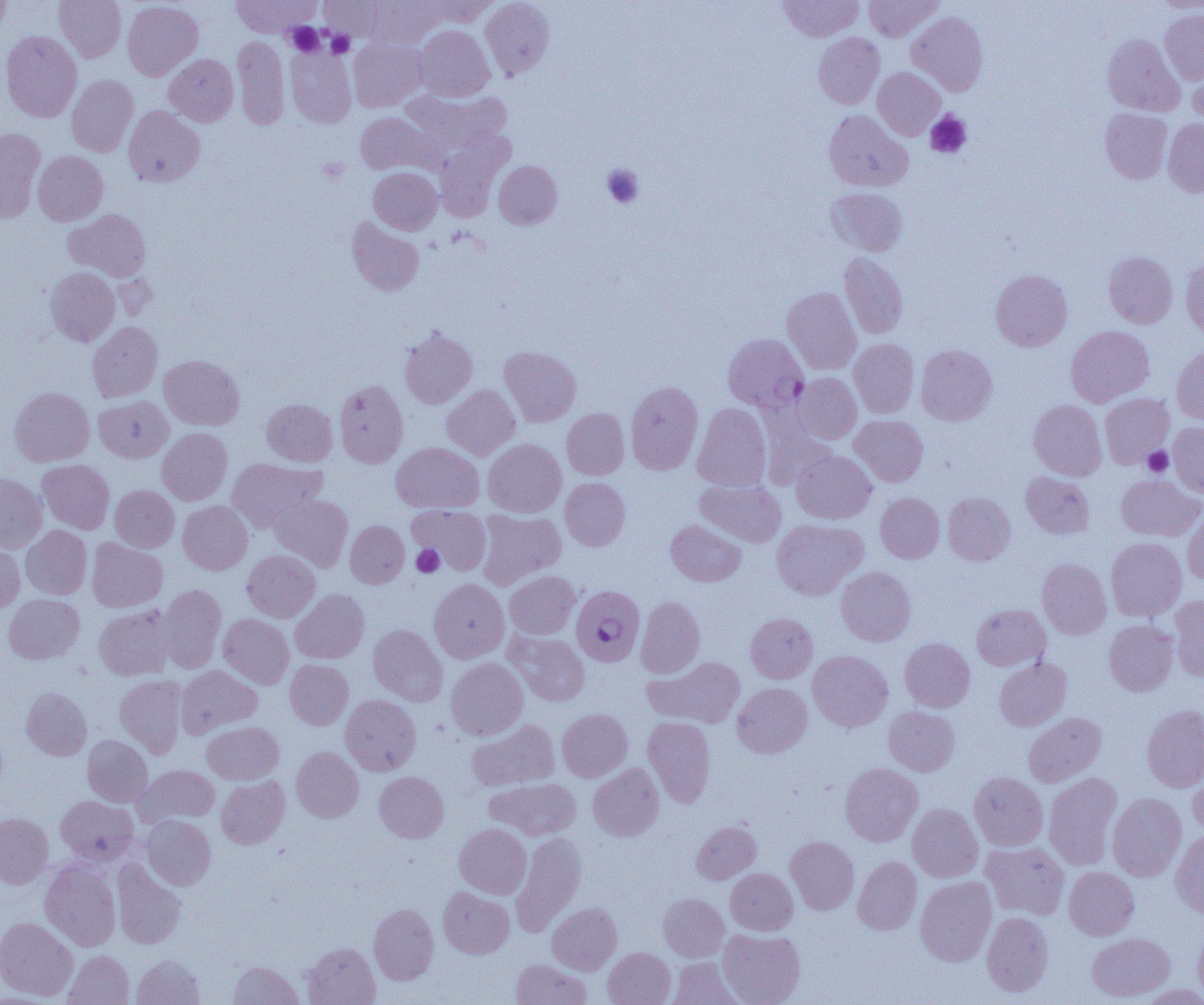

Summary:
  - Coordinate format: approximate bounding boxes as (x1, y1, x2, y2) in pixels
  - Uninfected red blood cell locations: (0, 0, 11, 40), (54, 0, 126, 62), (230, 0, 319, 37), (320, 0, 389, 41), (480, 0, 555, 80), (778, 0, 863, 41), (864, 0, 943, 40), (1153, 0, 1204, 12), (123, 1, 203, 80), (366, 1, 446, 49), (422, 1, 499, 26), (1160, 9, 1204, 85), (907, 12, 988, 96), (415, 26, 494, 101), (1, 31, 82, 122), (813, 32, 884, 109), (1102, 34, 1184, 116), (232, 36, 289, 130), (349, 38, 428, 112), (285, 45, 357, 128), (164, 54, 238, 126), (1187, 62, 1204, 126), (873, 67, 945, 140), (66, 74, 139, 157), (404, 89, 511, 155), (123, 105, 205, 187), (1100, 108, 1173, 184), (824, 110, 912, 191), (355, 112, 439, 175), (1163, 119, 1204, 197), (0, 128, 45, 222), (435, 138, 510, 222), (33, 151, 108, 225), (494, 160, 562, 229), (368, 167, 441, 234), (827, 187, 908, 257), (65, 209, 151, 280), (347, 217, 424, 296), (1103, 251, 1178, 328), (839, 253, 908, 339), (1180, 255, 1204, 337), (45, 267, 120, 346), (991, 269, 1072, 351), (782, 287, 861, 374), (87, 322, 163, 402), (1065, 326, 1154, 407), (399, 327, 478, 408), (849, 338, 919, 417), (1171, 343, 1204, 425), (916, 345, 997, 425), (499, 346, 581, 426), (159, 354, 244, 430), (793, 373, 862, 444), (334, 379, 408, 468), (626, 381, 703, 474), (442, 384, 520, 460), (9, 387, 94, 466), (1100, 393, 1174, 468), (94, 396, 173, 462), (262, 399, 337, 466), (1028, 399, 1107, 480), (692, 403, 772, 491), (562, 408, 629, 479), (850, 415, 928, 487), (1168, 421, 1204, 496), (157, 427, 232, 505), (483, 439, 566, 517), (391, 442, 484, 513), (791, 450, 876, 524), (227, 457, 325, 532), (37, 459, 114, 533), (1020, 472, 1095, 539), (0, 473, 47, 553), (1115, 474, 1203, 541), (560, 477, 630, 550), (695, 478, 786, 547), (110, 485, 179, 552), (875, 492, 944, 563), (943, 492, 1015, 565), (270, 493, 353, 571), (178, 501, 252, 574), (408, 505, 491, 575), (476, 509, 566, 589), (1183, 509, 1204, 585), (666, 519, 746, 586), (771, 519, 867, 600), (345, 520, 409, 588), (21, 525, 92, 600), (1106, 537, 1187, 621), (87, 538, 167, 612), (0, 541, 25, 613), (242, 550, 320, 622), (1037, 557, 1111, 639), (836, 566, 916, 646), (504, 571, 580, 639), (429, 579, 509, 663), (158, 584, 226, 673), (291, 588, 370, 664), (3, 594, 84, 664), (636, 596, 705, 678), (1169, 596, 1204, 680), (972, 604, 1050, 670), (94, 605, 175, 680), (218, 613, 294, 688), (746, 613, 817, 683), (1104, 619, 1178, 696), (368, 625, 447, 705), (508, 632, 589, 706), (899, 638, 975, 712), (807, 650, 893, 732), (645, 656, 745, 728), (446, 658, 528, 740), (994, 658, 1071, 731), (285, 659, 353, 729), (176, 665, 262, 737), (115, 675, 188, 758), (733, 682, 812, 758), (21, 687, 92, 760), (340, 694, 421, 775), (1141, 704, 1204, 792), (884, 706, 960, 776), (557, 708, 632, 781), (1023, 712, 1106, 787), (643, 716, 715, 807), (467, 719, 560, 791), (202, 721, 284, 784), (82, 735, 153, 806), (291, 746, 364, 822), (1187, 761, 1204, 838), (840, 762, 922, 846), (588, 763, 664, 841), (134, 765, 220, 826), (374, 771, 449, 843), (969, 771, 1048, 851), (1043, 772, 1123, 870), (216, 776, 290, 849), (486, 777, 580, 840), (1107, 792, 1186, 881), (56, 795, 138, 864), (907, 804, 983, 882), (0, 813, 53, 888), (142, 815, 216, 889), (691, 820, 761, 884), (454, 823, 532, 899), (1171, 829, 1204, 919), (511, 832, 586, 936), (785, 836, 859, 914), (981, 842, 1069, 919), (853, 856, 922, 935), (112, 859, 186, 949), (40, 860, 121, 951), (1064, 867, 1139, 940), (725, 868, 798, 935), (915, 877, 996, 966), (438, 887, 515, 958), (658, 893, 729, 961), (369, 903, 439, 984), (547, 903, 622, 975), (981, 912, 1053, 996), (0, 917, 78, 1001), (1193, 927, 1204, 1003), (718, 929, 805, 1005), (1086, 932, 1174, 1002), (303, 942, 381, 1005), (603, 948, 675, 1005), (63, 950, 134, 1005), (132, 955, 204, 1005), (669, 958, 744, 1004), (510, 959, 591, 1005), (229, 960, 303, 1005), (1138, 984, 1204, 1004)
  - Plasmodium falciparum-infected red blood cell locations: (723, 333, 808, 412), (569, 586, 644, 665)
  - Platelet locations: (286, 22, 324, 55), (326, 30, 355, 58), (925, 111, 972, 158), (317, 157, 349, 183), (602, 164, 644, 209), (1142, 446, 1173, 477), (411, 544, 443, 577)
  - Slide-level diagnosis: Plasmodium falciparum
  - Modality: light microscopy
  - Image size: 1204×1005 pixels
  - Field of view: single
  - Preparation: thin blood film
  - Magnification: 1000x